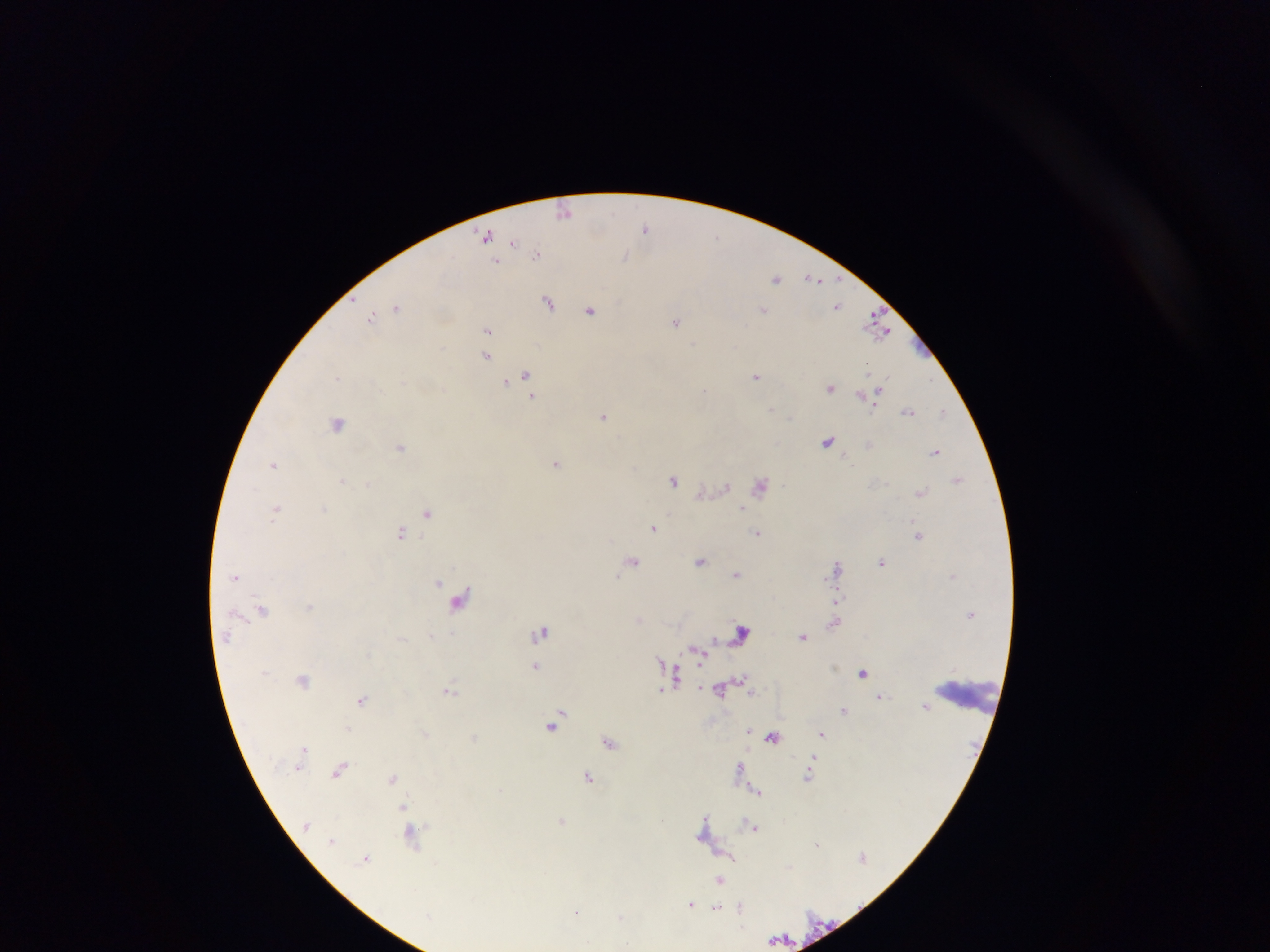
capture = mobile-phone photograph through a microscope
field of view = single
preparation = thick blood smear
malaria parasite locations = approximate centers as x y in pixels: 565 211; 646 227; 485 235; 716 235; 514 241; 537 254; 625 256; 497 261; 777 278; 812 278; 548 302; 838 305; 396 307; 591 310; 763 310; 372 317; 676 321; 877 324; 487 330; 694 344; 486 355; 526 376; 756 376; 337 377; 505 382; 831 387; 705 390; 532 396; 771 409; 908 410; 943 411; 604 415; 790 416; 337 423; 828 440; 400 447; 936 451; 556 462; 273 463; 342 479; 958 479; 674 480; 368 484; 725 486; 760 486; 920 492; 276 509; 324 509; 741 509; 427 512; 653 528; 401 532; 758 533; 918 535; 633 560; 701 560; 882 561; 837 566; 736 574; 236 576; 439 583; 459 599; 837 599; 310 606; 262 609; 639 620; 834 623; 542 631; 742 632; 431 635; 802 636; 227 637; 714 640; 661 660; 701 660; 536 666; 863 673; 676 676; 740 678; 303 680; 449 690; 661 690; 720 690; 751 692; 881 696; 363 700; 926 706; 845 711; 560 713; 553 725; 348 729; 749 730; 426 733; 822 733; 773 736; 475 737; 610 742; 813 759; 740 768; 341 769; 809 775; 589 776; 392 778; 757 790; 404 806; 705 818; 562 820; 753 826; 412 834; 332 841; 817 843; 366 858; 720 880; 690 904; 716 908; 741 908; 576 912; 620 917
image size = 1270×952 pixels
country = Ghana
leukocyte locations = approximate centers as x y in pixels: 970 696